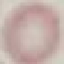
malaria_status: uninfected
capture: smartphone camera at the microscope eyepiece
image_type: automatically extracted cell patch, resized to 64 × 64 pixels
stain: Giemsa
preparation: thin smear